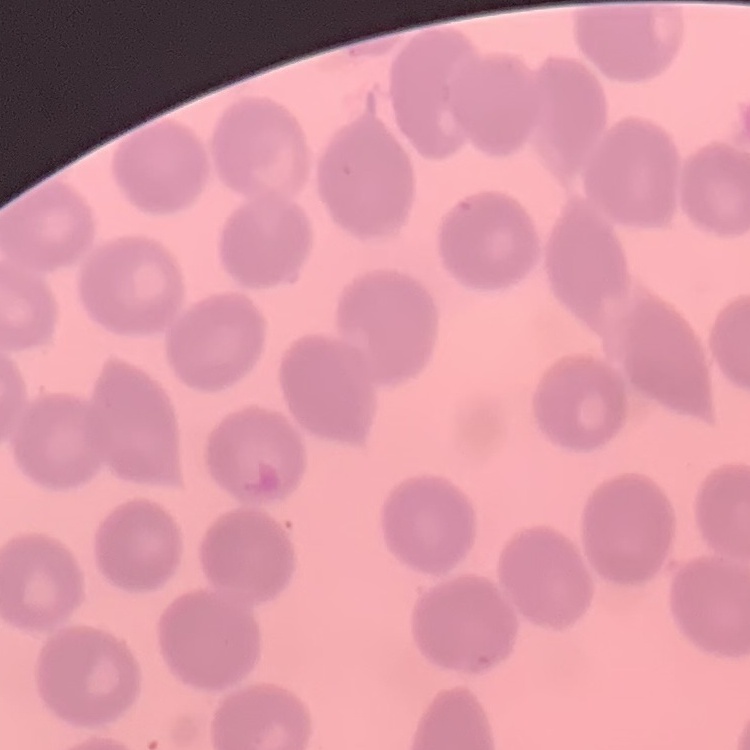
red blood cell morphology = no rouleaux formation
image type = one tile cut from a larger photomicrograph
stain = Field's or Giemsa
preparation = thin blood smear